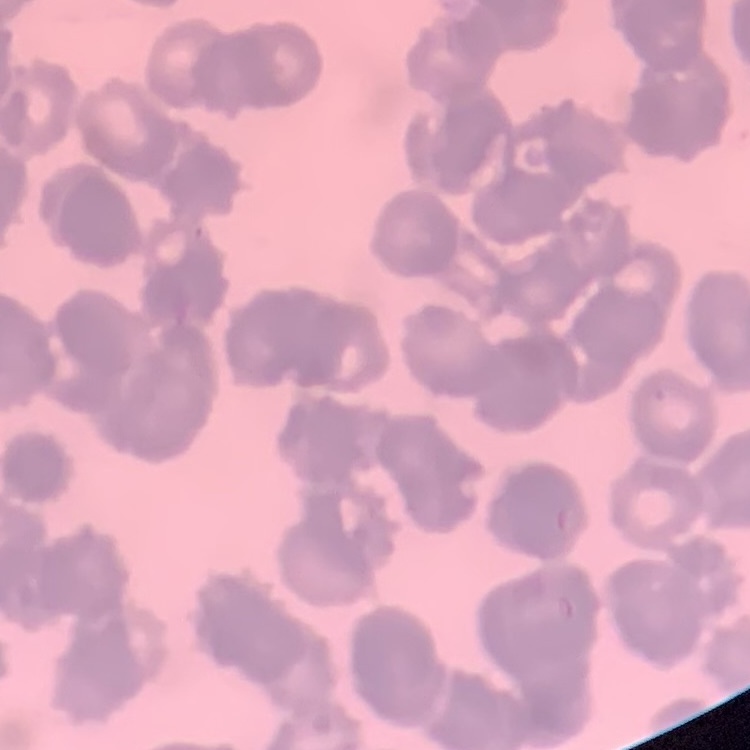
The erythrocytes exhibit rouleaux formation. Thin blood smear. Stained with either Field's or Giemsa. Square crop of a larger photomicrograph.